Classify this cell by malaria status.
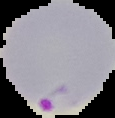

It is parasitized.

Image is 115×118 pixels. From a thin blood smear. Segmented cell region on a black background.